Locate every leukocyte (white blood cell).
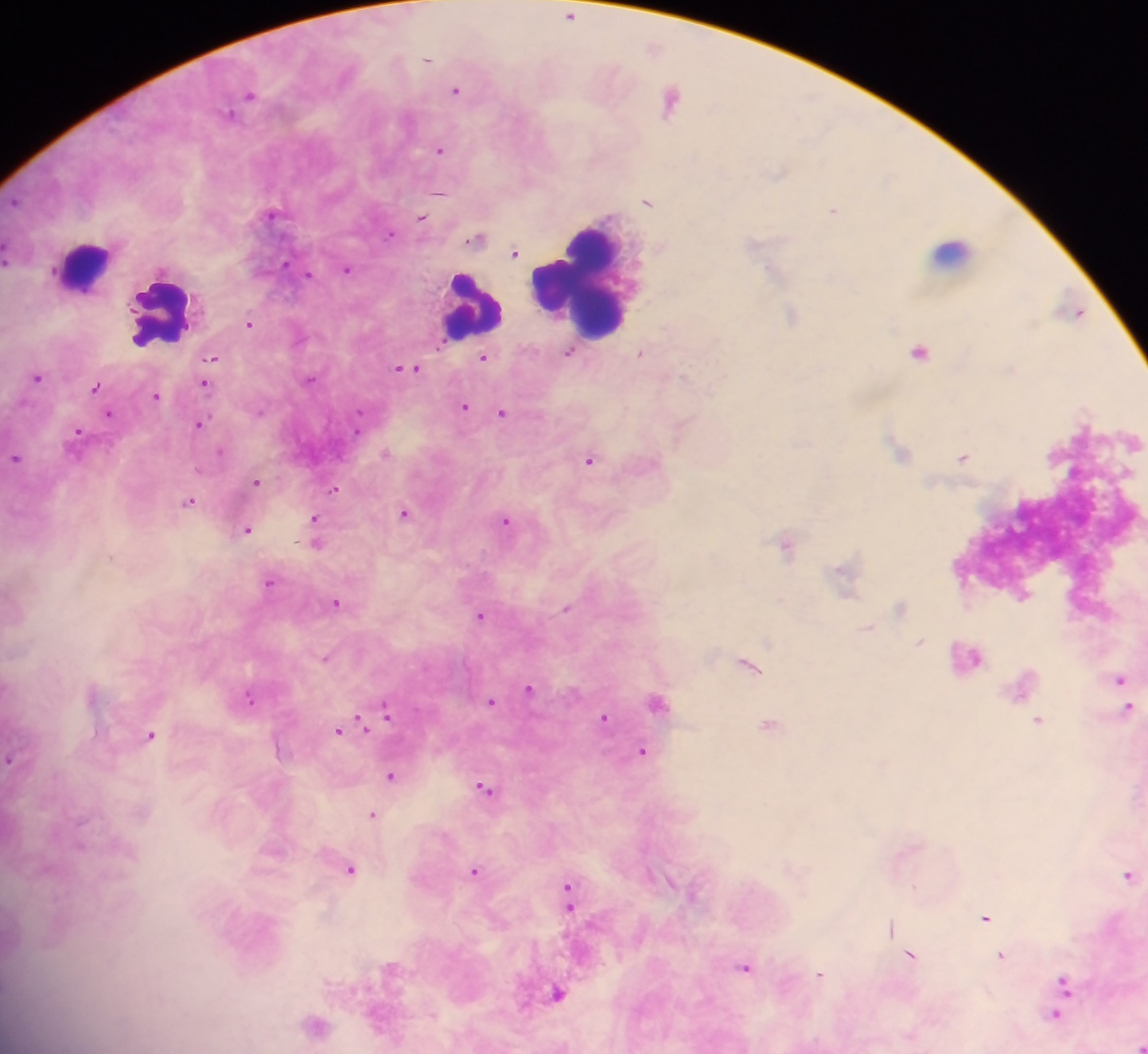

Approximate centers as x y in pixels.
Leukocytes: 951 250; 82 264; 579 275; 474 310; 164 316.

Malaria parasite locations: 570 16; 428 59; 456 90; 250 95; 671 100; 230 113; 440 150; 780 174; 440 192; 647 201; 834 210; 271 214; 421 218; 389 234; 476 239; 515 253; 285 263; 347 269; 771 272; 309 274; 1077 312; 792 315; 250 324; 569 352; 920 352; 642 353; 212 357; 484 357; 407 368; 684 375; 37 377; 311 379; 205 383; 95 386; 156 397; 464 407; 260 412; 108 413; 502 413; 200 424; 77 432; 897 448; 221 451; 387 452; 963 457; 15 458; 589 460; 257 482; 335 489; 189 501; 405 514; 315 520; 505 521; 248 530; 315 531; 317 544; 787 544; 269 582; 337 602; 566 608; 480 614; 867 628; 919 642; 325 657; 748 664; 1119 680; 529 688; 249 698; 492 701; 658 701; 1127 709; 386 711; 604 717; 1038 721; 364 722; 361 723; 769 725; 340 729; 151 735; 643 752; 11 759; 392 775; 485 788; 373 815; 351 870; 474 872; 1129 874; 568 895; 986 918; 890 926; 910 956; 1001 957; 745 968; 820 975; 1063 989; 556 994; 1058 1010; 1138 1044. Mobile-phone photograph taken through the microscope. Sample from Ghana. One field of view. Thick blood smear. Image is 1148×1054 pixels.